Assess this cell for malaria.
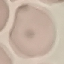
It is uninfected.

{
  "stain": "Giemsa",
  "preparation": "thin blood smear",
  "image_type": "cell patch, automatically extracted from a larger field of view and resized to 64 × 64 pixels",
  "capture": "smartphone through the microscope eyepiece"
}